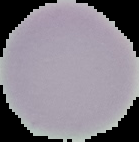

Cell region segmented out of the field of view; the surrounding area is masked to black. From a thin blood film. Malaria status: uninfected. Image is 139×142 pixels.